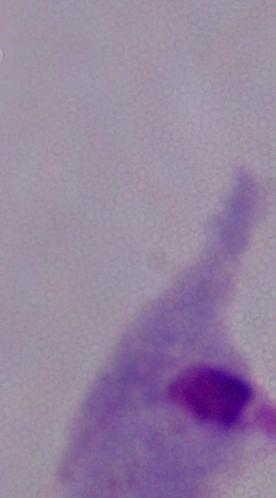

{
  "identification": "trichomonad",
  "magnification": "1000x",
  "modality": "micrograph"
}